Identify the blood parasite species.
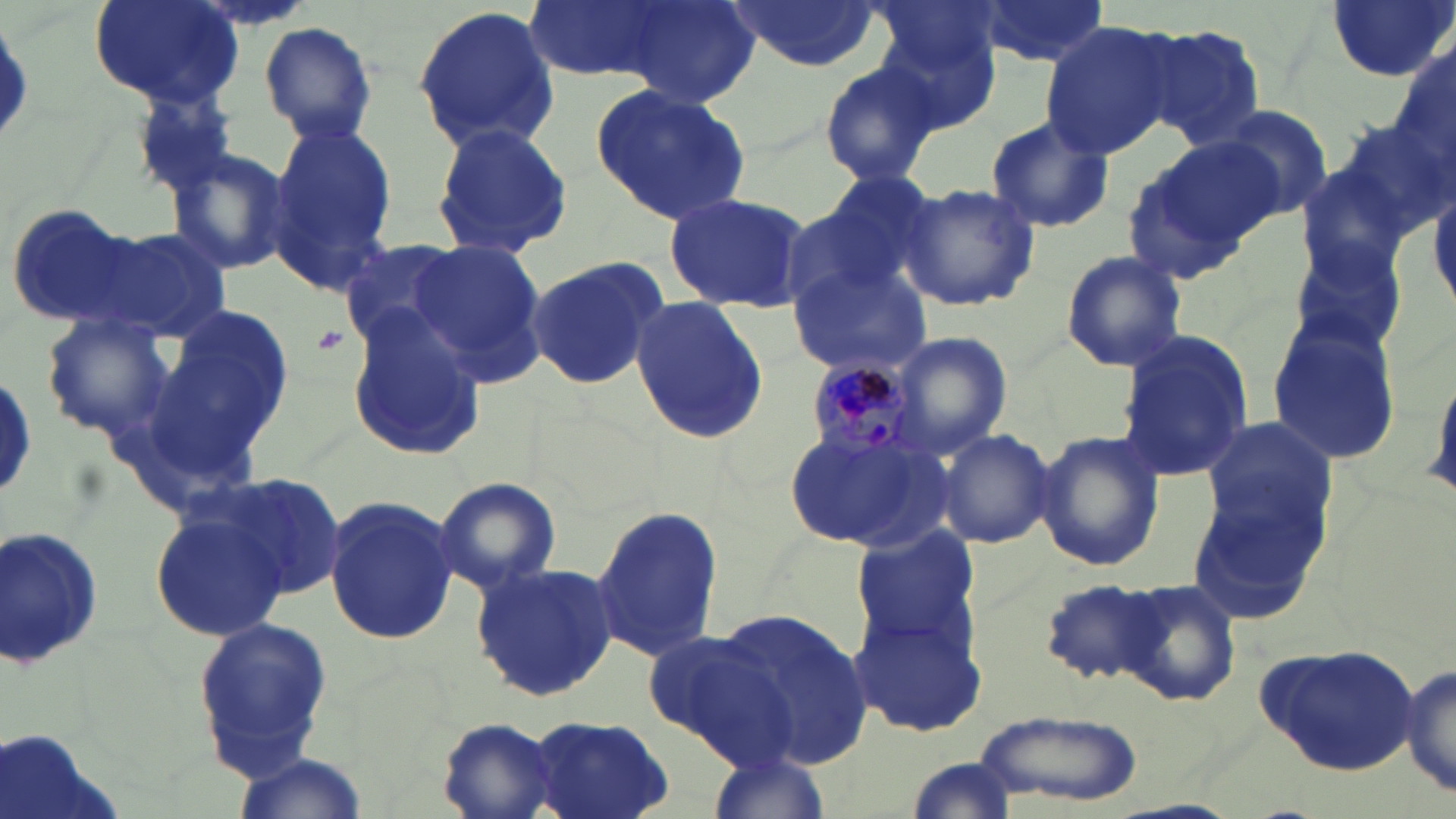

Plasmodium malariae.

Summary:
  - Coordinate format: approximate bounding boxes as (x1,y1)-(x2,y2) corner pairs in pixels
  - Platelet locations: (310,323)-(354,360)
  - Uninfected red blood cell locations (subset): (90,0)-(243,108), (522,0)-(677,82), (604,0)-(762,108), (972,0)-(1107,66), (1325,0)-(1453,82), (725,1)-(883,71), (411,5)-(560,152), (870,14)-(1002,136), (1038,21)-(1178,159), (261,22)-(378,144), (1136,22)-(1268,149), (1391,45)-(1454,177), (816,57)-(944,187), (590,81)-(750,225), (1204,106)-(1333,223), (984,114)-(1114,234), (263,117)-(399,290), (1323,119)-(1453,257), (430,121)-(575,257), (1126,136)-(1279,276), (166,149)-(293,277), (1295,161)-(1416,287), (787,171)-(942,317), (1430,181)-(1456,311), (899,182)-(1040,314), (662,190)-(812,313), (5,202)-(140,325), (92,224)-(233,344), (339,239)-(472,351), (407,239)-(549,386), (1059,249)-(1188,374), (521,253)-(671,392), (788,258)-(935,382), (627,298)-(771,441), (156,309)-(295,452), (344,309)-(487,463), (40,315)-(174,442), (1267,316)-(1404,469), (1115,329)-(1252,480), (892,330)-(1016,455), (1425,359)-(1456,510), (1195,420)-(1342,559), (780,422)-(947,553), (936,428)-(1057,548), (1033,428)-(1166,573), (1188,462)-(1335,630), (218,471)-(346,599), (431,474)-(563,595), (322,493)-(459,647), (151,504)-(289,643), (591,506)-(727,663), (1,522)-(103,672), (848,523)-(981,655), (469,562)-(619,703), (1038,579)-(1171,687), (1115,580)-(1242,707), (848,603)-(987,736), (714,608)-(875,770), (189,615)-(335,783), (640,629)-(793,763), (1402,661)-(1456,801), (976,710)-(1144,807), (527,712)-(676,817), (438,718)-(564,817), (0,729)-(120,819), (708,750)-(828,819), (231,752)-(364,818), (902,757)-(1020,818)
  - Plasmodium malariae-infected red blood cell locations: (806,361)-(921,463)
  - Magnification: 1000x
  - Preparation: thin blood film
  - Field of view: one of a larger specimen
  - Stain: May-Grünwald-Giemsa
  - Modality: optical microscopy
  - Image size: 1456×819 pixels